Identify the parasite.
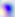
Toxoplasma gondii.

modality = photomicrograph
magnification = 400x